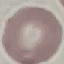
{
  "result": "no malaria parasites seen",
  "stain": "Giemsa",
  "capture": "smartphone through the microscope eyepiece",
  "preparation": "thin blood film",
  "image_type": "cell patch, automatically extracted from a larger field of view and resized to 64 × 64 pixels"
}